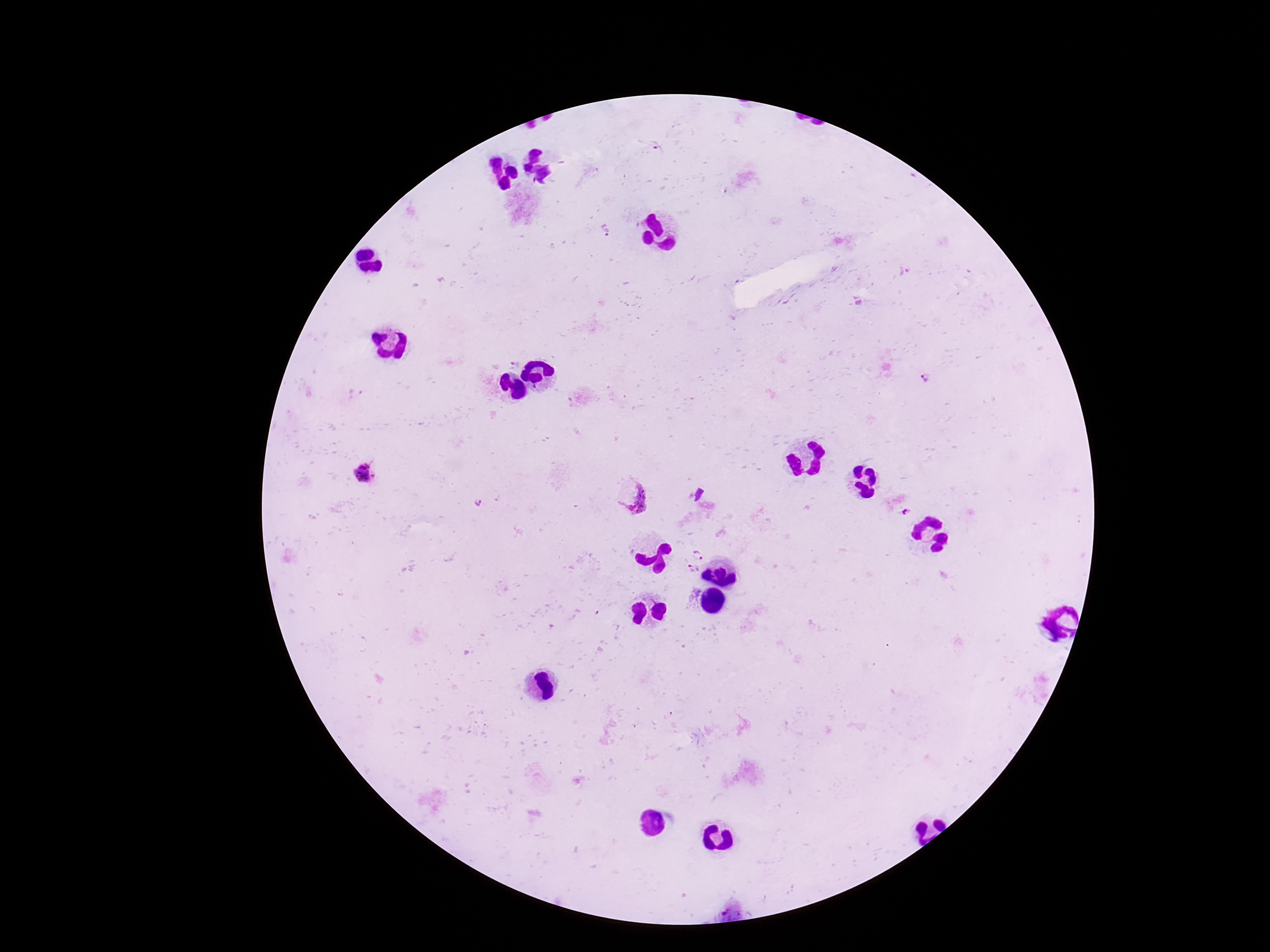
capture = smartphone camera through the microscope eyepiece
patient malaria status = infected
stain = Giemsa
field of view = single
Plasmodium parasite locations = approximate centers as (x, y) in pixels: (605, 231), (927, 379), (362, 474), (631, 493), (479, 501), (698, 554), (694, 569)
magnification = 100x
preparation = thick peripheral-blood smear
image size = 1270×952 pixels